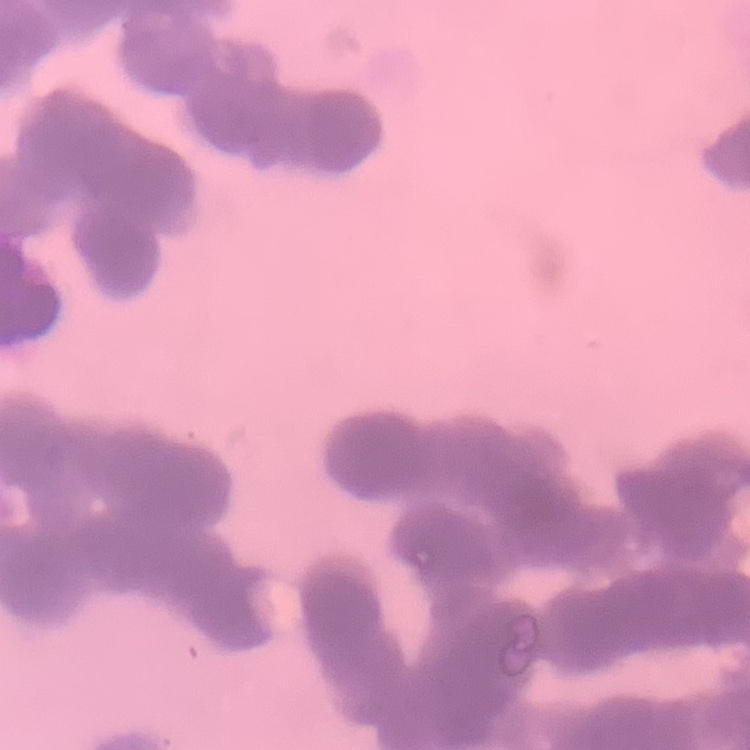 The erythrocytes exhibit rouleaux formation. Thin blood smear. Field's or Giemsa stain. Square crop of a larger photomicrograph.